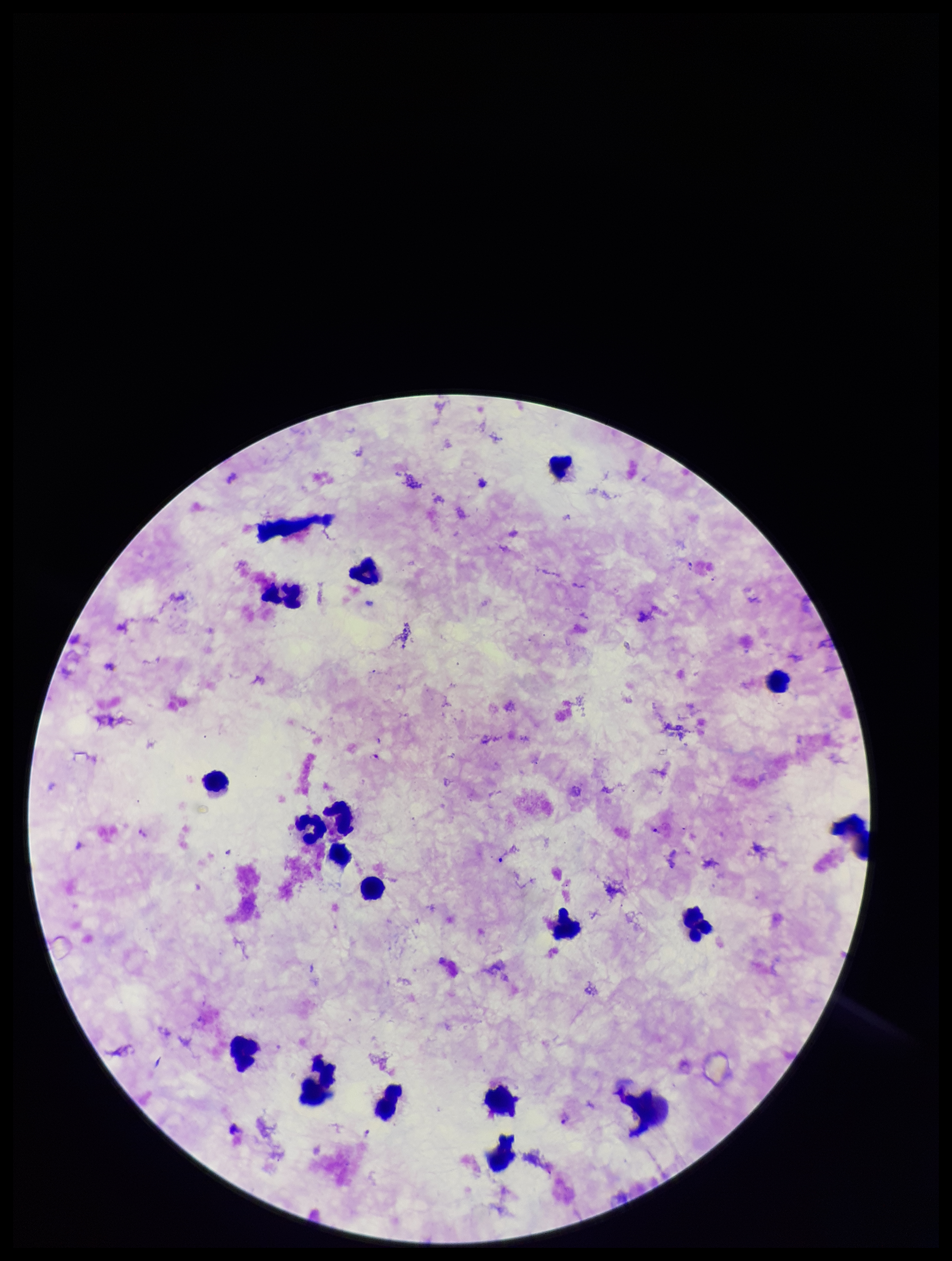
patient malaria status = infected
stain = Giemsa
field of view = one from this slide
capture = smartphone photograph through the microscope eyepiece
image size = 952×1261 pixels
parasite count = 3
Plasmodium parasites = detected
leukocyte count = 18
preparation = thick smear
species reported for this patient = Plasmodium falciparum